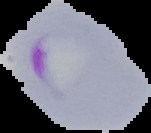
Image is 151×133 pixels. From a thin blood film. Segmented cell region on a black background. Malaria status: parasitized.